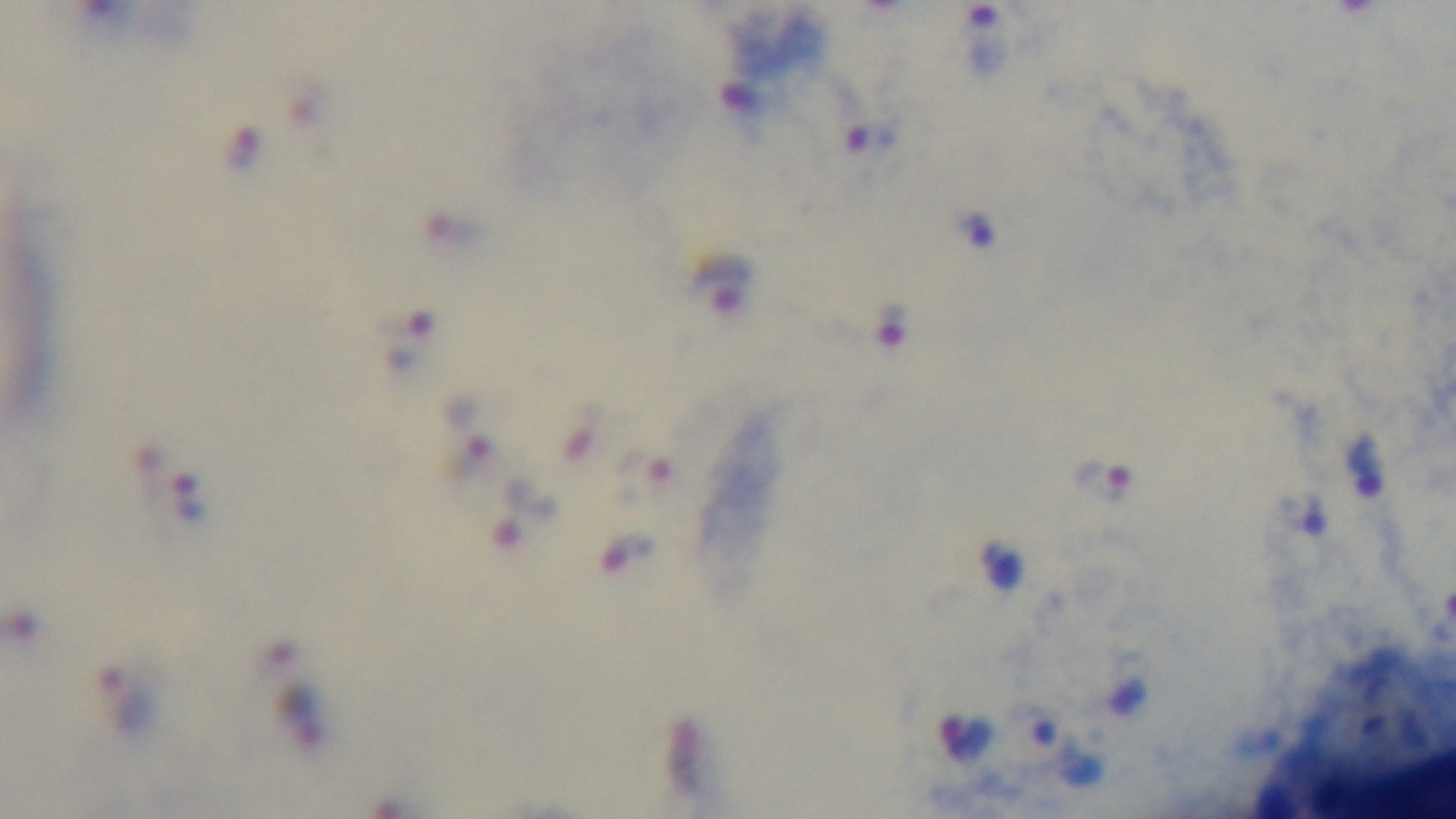
objective: 100x oil immersion
malaria_status: positive
field_of_view: single
modality: light microscopy
preparation: thick blood film
stain: Giemsa
capture: mounted 4K digital camera